Give the position of every Plasmodium parasite visible.
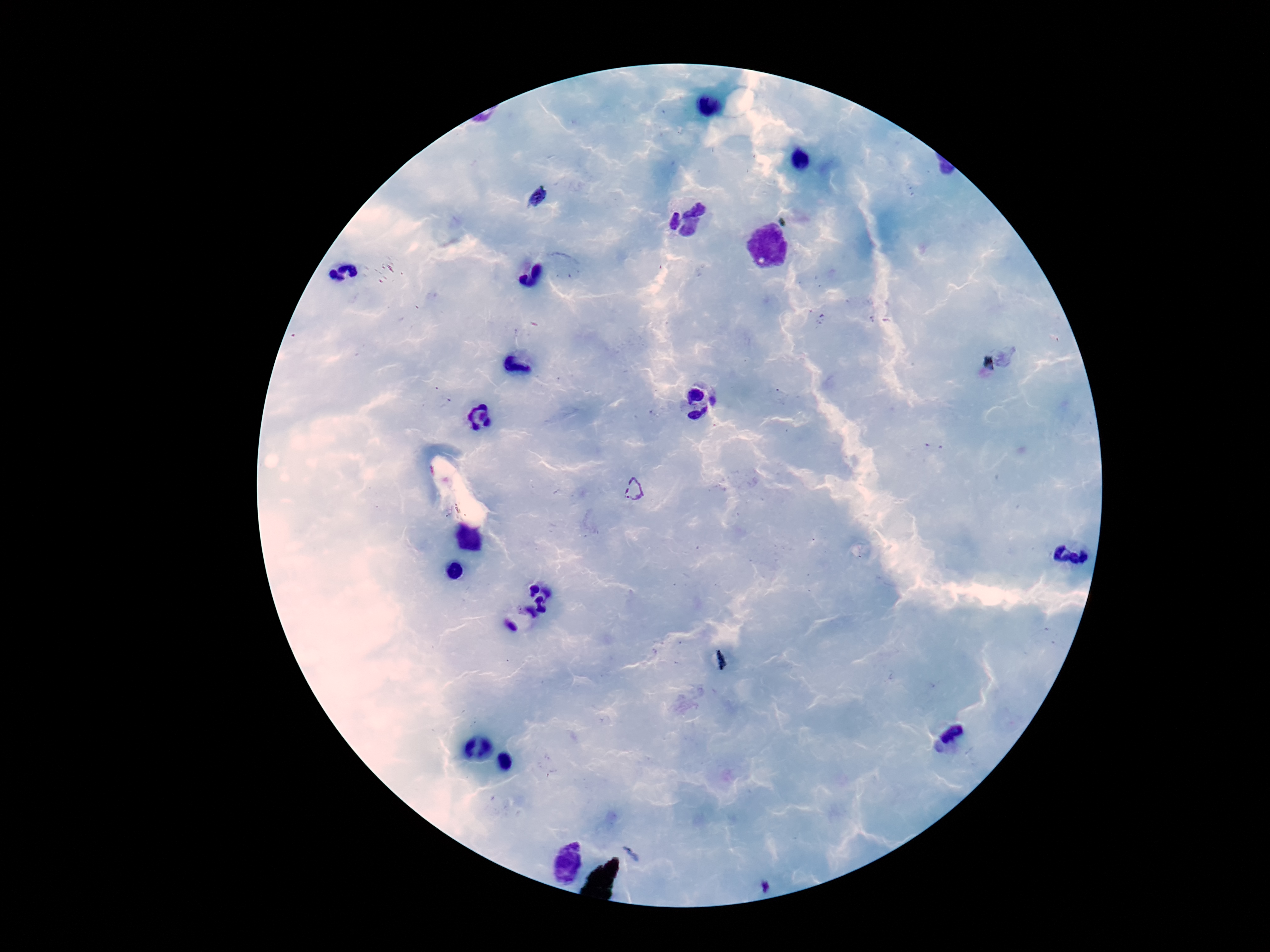
Approximate centers as (x, y) in pixels.
Plasmodium parasites: (538, 198), (632, 490).

magnification = 100x
stain = Giemsa
patient malaria status = positive
capture = smartphone camera through the microscope eyepiece
field of view = one from this slide
preparation = thick peripheral-blood smear
image size = 1270×952 pixels